Assess this cell for malaria.
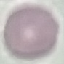

It is uninfected.

Summary:
  - Image type: cell patch, automatically extracted from a larger field of view and resized to 64 × 64 pixels
  - Capture: smartphone through the microscope eyepiece
  - Stain: Giemsa
  - Preparation: thin blood smear